Locate the red blood cells and classify each one as P. falciparum-infected, uninfected, or of indeterminate infection status.
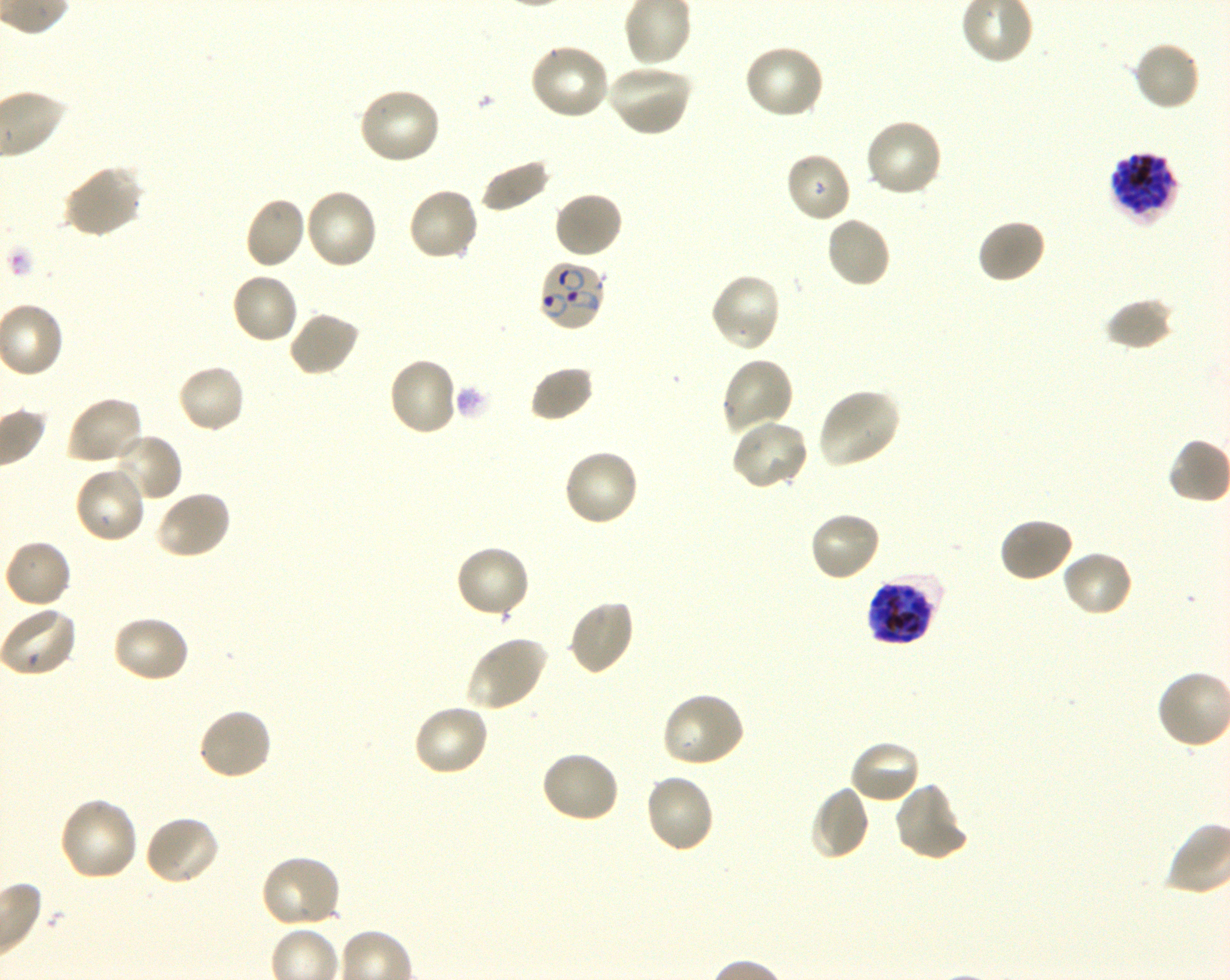
Approximate bounding boxes as (x1, y1, x2, y2) in pixels. Not every red blood cell is marked. A life-cycle stage — or a range of stages, where the recorded stages span more than one — follows each staged infected red blood cell.
Infected red blood cells: (1108, 152, 1180, 225) schizont; (537, 259, 608, 333) ring; (866, 574, 942, 646) late trophozoite to late schizont.
Uninfected red blood cells: (1132, 39, 1201, 111), (528, 42, 612, 122), (741, 43, 826, 120), (604, 63, 694, 138), (357, 86, 443, 166), (864, 118, 944, 199), (784, 152, 852, 224), (479, 160, 552, 213), (61, 165, 144, 238), (406, 186, 481, 263), (303, 188, 379, 271), (553, 190, 624, 260), (244, 196, 307, 270), (825, 215, 892, 289), (976, 218, 1047, 285), (230, 272, 300, 345), (708, 272, 783, 353), (1105, 296, 1176, 351), (286, 310, 361, 378), (387, 356, 459, 437), (720, 357, 796, 436), (176, 362, 246, 434), (530, 365, 595, 422), (816, 386, 901, 469), (66, 397, 146, 466), (729, 418, 809, 492), (108, 432, 183, 503), (562, 448, 641, 528), (74, 465, 148, 545), (154, 488, 232, 560), (808, 510, 882, 583), (997, 516, 1075, 584), (3, 538, 72, 609), (454, 545, 532, 620), (1060, 549, 1134, 618), (567, 598, 636, 676), (0, 604, 78, 677), (111, 614, 191, 684), (463, 634, 549, 712), (660, 691, 747, 770), (411, 703, 491, 778), (196, 706, 274, 782), (847, 739, 922, 805), (540, 750, 621, 825), (643, 773, 716, 854), (893, 780, 969, 862), (809, 785, 870, 862), (57, 796, 140, 883), (143, 813, 221, 886), (258, 854, 342, 929).
No red blood cells of indeterminate infection status observed.

Giemsa-stained preparation. Life-cycle stages observed: ring, schizont. P. falciparum strain 3D7 in shaking in-vitro culture. Image is 1230×980 pixels. Single field of view. 100x objective under oil immersion, numerical aperture 1.30. Blood group of the donor: O+. Thin blood smear.